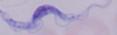 1000x magnification. Micrograph. A trypanosome is seen.